Mark where leukocytes are.
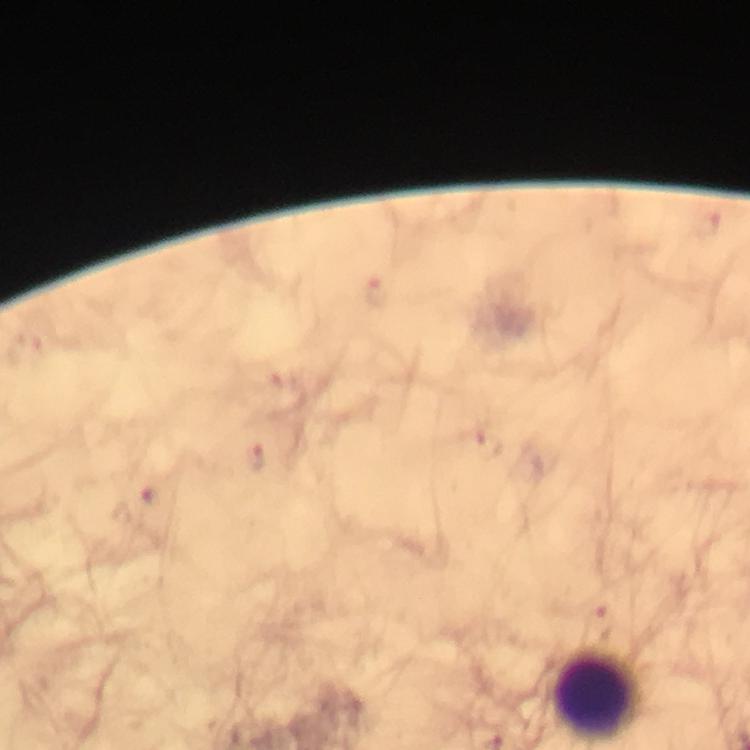

Approximate object centers, in pixels from the top-left corner.
Leukocytes: (x=602, y=697).

{
  "immersion_oil": "applied",
  "image_size": "750×750 pixels",
  "malaria_parasite_locations": "approximate object centers, in pixels from the top-left corner: (x=376, y=288), (x=487, y=445), (x=258, y=458), (x=601, y=622)",
  "stain": "Giemsa",
  "magnification": "100x",
  "capture": "smartphone photograph through a microscope",
  "preparation": "thick blood film",
  "cropped_from": "one field of view",
  "context": "from a diagnostic examination for malaria"
}